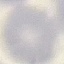

Summary:
  - Malaria status: uninfected
  - Image type: automatically extracted cell patch, resized to 64 × 64 pixels
  - Capture: smartphone through the microscope eyepiece
  - Preparation: thin blood smear
  - Stain: Giemsa